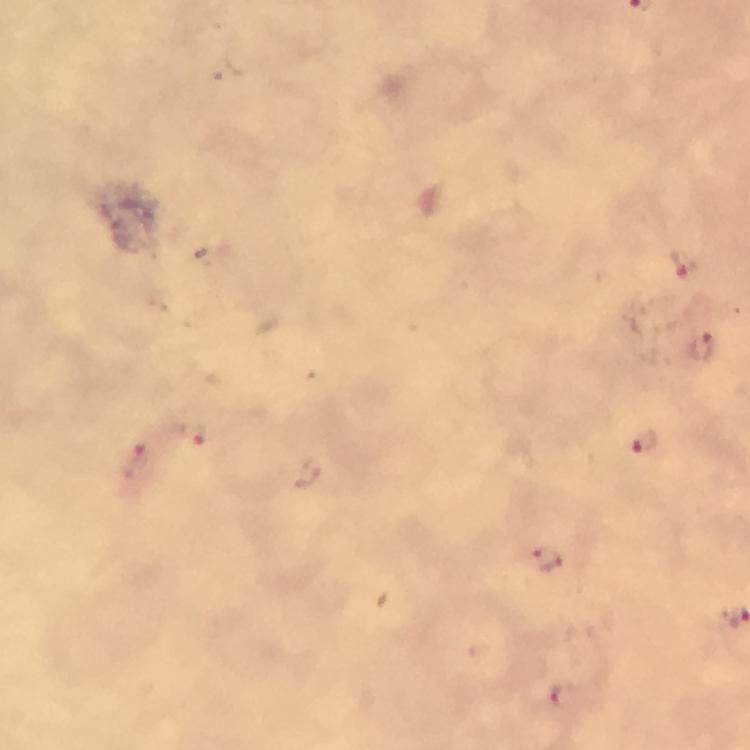

magnification = 100x
cropped from = one field of view
context = from a diagnostic examination for malaria
image size = 750×750 pixels
capture = smartphone mounted on the microscope
stain = Giemsa
immersion oil = applied
preparation = thick blood film
malaria parasite locations = approximate object centers, in pixels from the top-left corner: (x=683, y=264), (x=700, y=347), (x=193, y=434), (x=644, y=442), (x=135, y=465), (x=548, y=560), (x=558, y=693)